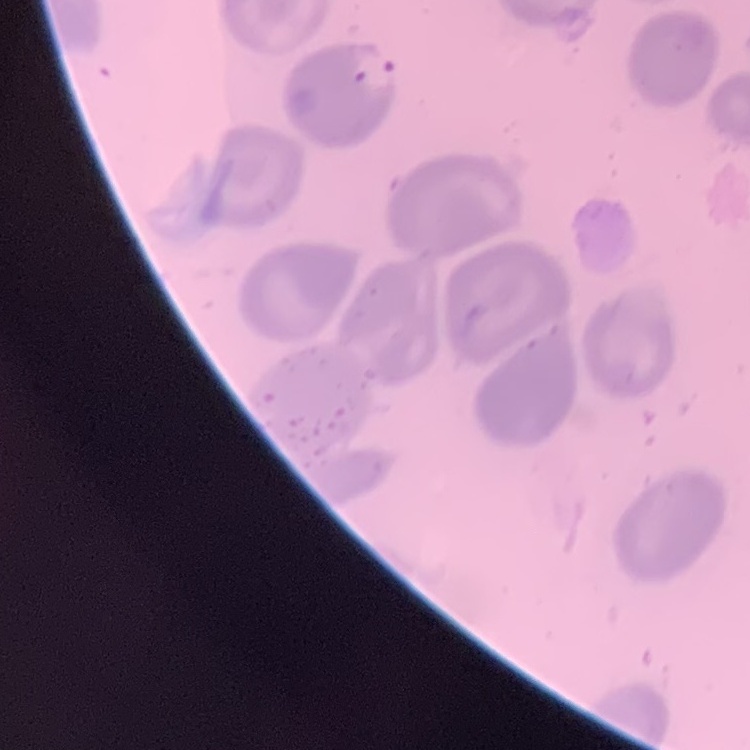

erythrocyte_morphology: no rouleaux formation
preparation: thin peripheral smear
stain: Field's or Giemsa
image_type: square crop of a larger photomicrograph